Locate every uninfected red blood cell.
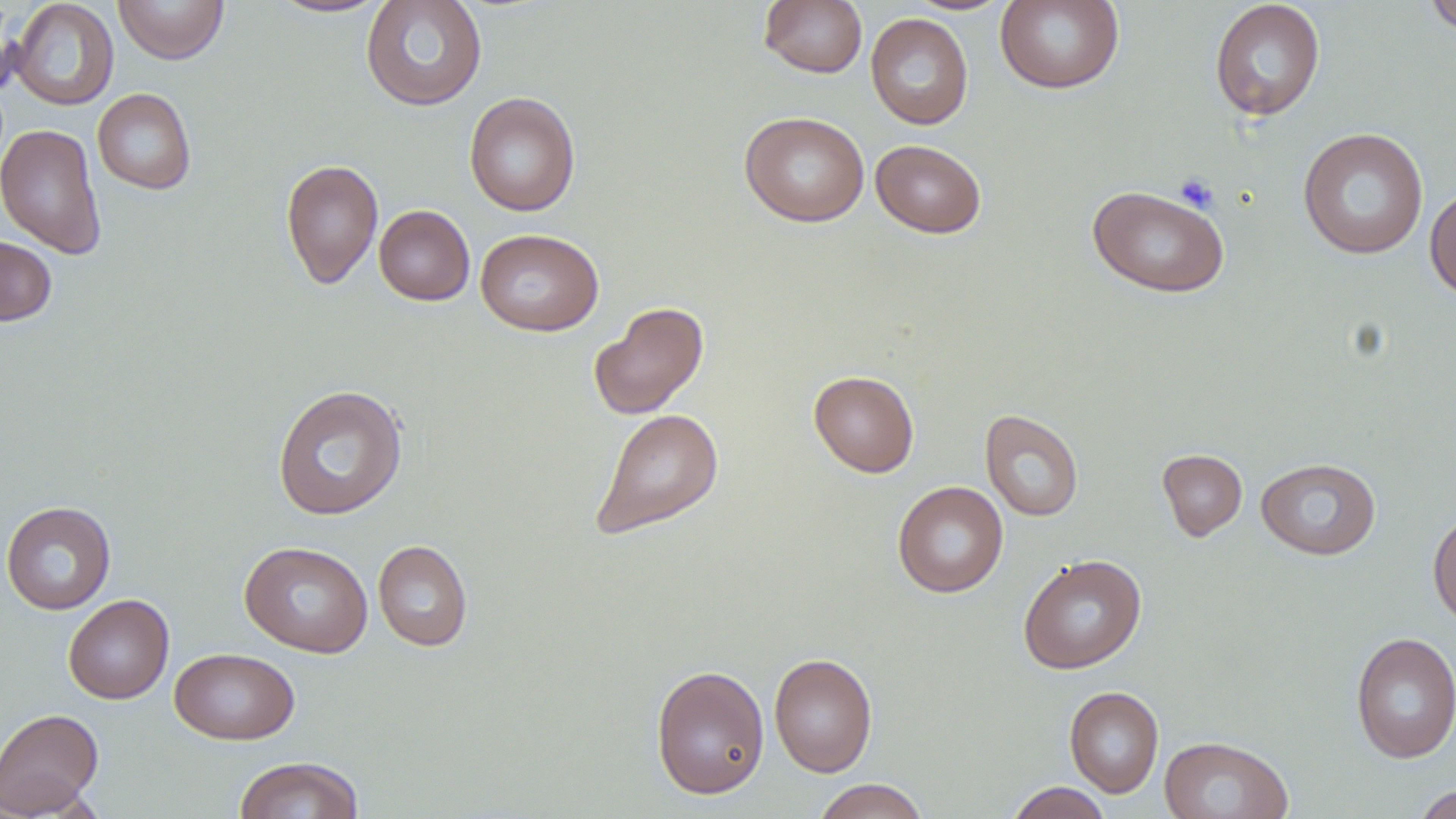

Approximate bounding boxes as (x1, y1, x2, y2) in pixels.
Uninfected red blood cells: (113, 0, 229, 64), (267, 0, 392, 19), (360, 0, 488, 111), (758, 0, 867, 78), (901, 0, 1017, 16), (995, 0, 1125, 94), (1423, 0, 1456, 37), (9, 1, 119, 111), (1209, 1, 1326, 121), (865, 13, 973, 130), (93, 88, 196, 194), (463, 91, 580, 217), (739, 111, 869, 227), (0, 123, 107, 259), (1298, 127, 1429, 259), (870, 139, 987, 239), (280, 158, 383, 289), (1088, 184, 1230, 298), (1424, 184, 1456, 301), (374, 205, 475, 306), (475, 228, 604, 336), (0, 234, 58, 325), (589, 302, 709, 420), (808, 370, 919, 477), (272, 385, 408, 520), (590, 408, 724, 541), (980, 409, 1084, 521), (1157, 449, 1247, 541), (1255, 457, 1381, 560), (892, 480, 1008, 598), (1, 500, 116, 615), (1428, 509, 1456, 629), (373, 539, 473, 651), (239, 541, 373, 657), (1018, 553, 1146, 674), (63, 594, 174, 704), (1349, 631, 1456, 764), (169, 648, 300, 745), (769, 652, 878, 777), (650, 664, 770, 800), (1064, 686, 1164, 798), (0, 707, 104, 817), (1159, 735, 1293, 819), (233, 756, 364, 818), (811, 779, 929, 819), (1006, 782, 1112, 818), (1412, 784, 1456, 819).

Summary:
  - Platelet locations: (1173, 172, 1222, 212)
  - Slide-level diagnosis: no evidence of blood parasites
  - Stain: May-Grünwald-Giemsa
  - Magnification: 1000x
  - Image size: 1456×819 pixels
  - Modality: optical microscopy
  - Field of view: one of a larger specimen
  - Preparation: thin blood smear